Assess this cell for malaria.
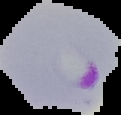
Parasitized.

From a thin blood smear. Segmented cell region on a black background. Image is 121×115 pixels.